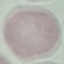
Summary:
  - Result: negative for malaria parasites
  - Stain: Giemsa
  - Preparation: thin blood smear
  - Capture: smartphone camera at the microscope eyepiece
  - Image type: automatically extracted cell patch, resized to 64 × 64 pixels